Describe the morphology of the red blood cells.
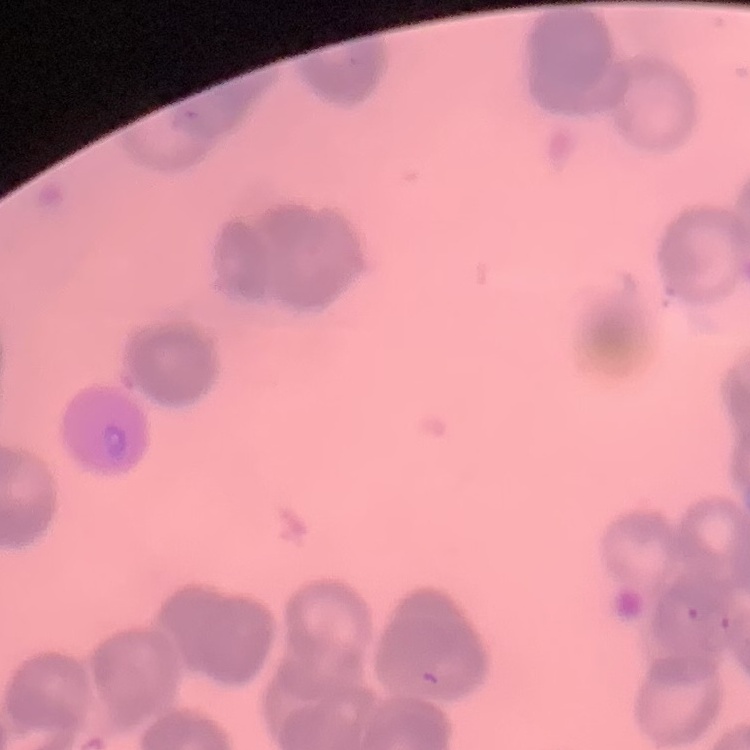

Rouleaux formation.

Summary:
  - Image type: square crop of a larger photomicrograph
  - Stain: Field's or Giemsa
  - Preparation: thin blood smear